Give the extent of all Plasmodium vivax-infected red blood cells.
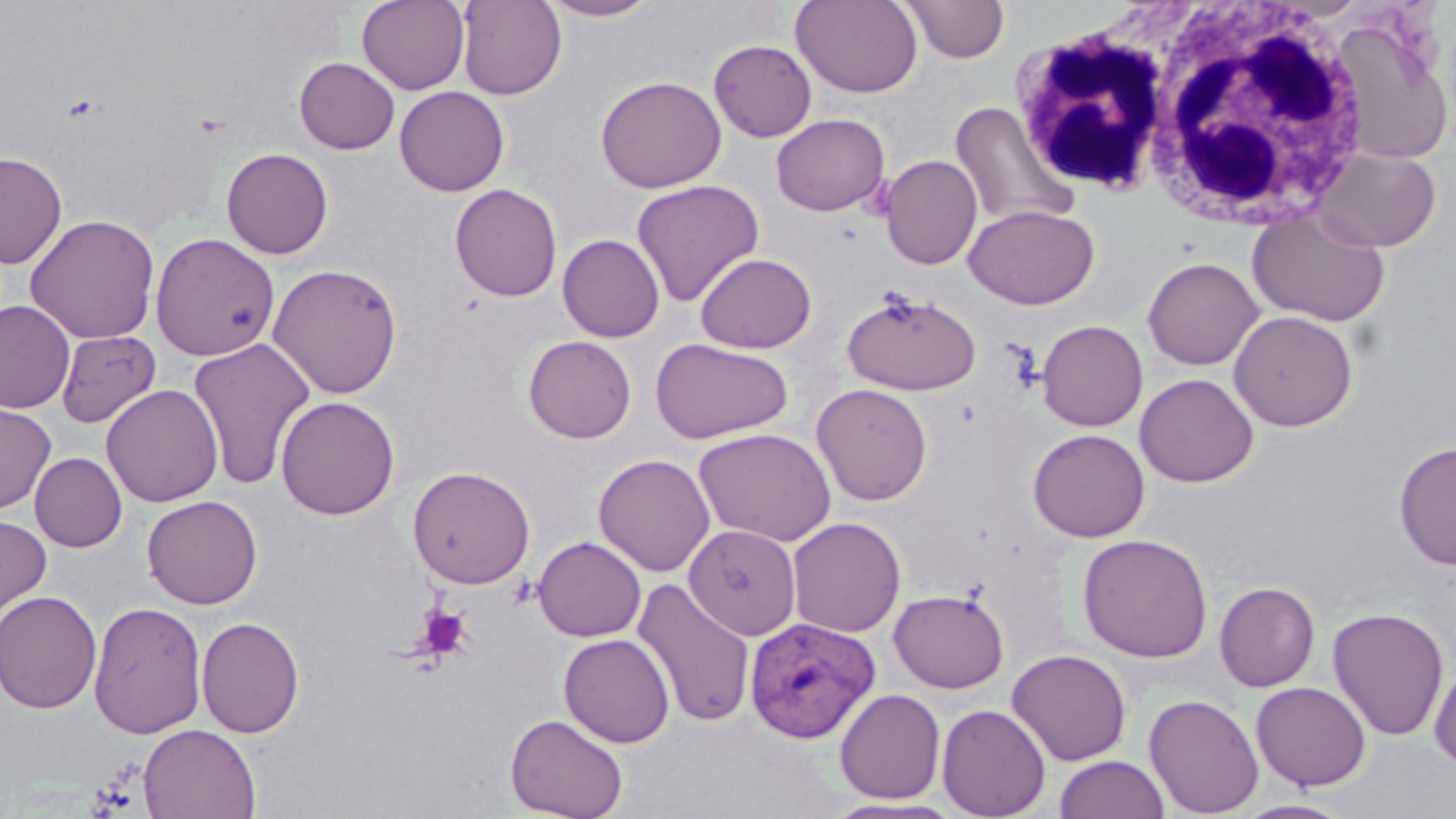

Approximate bounding boxes as [x1, y1, x2, y2] in pixels.
Plasmodium vivax-infected red blood cells: [744, 615, 883, 743].

{
  "slide_level_diagnosis": "Plasmodium vivax",
  "image_size": "1456×819 pixels",
  "magnification": "1000x",
  "uninfected_red_blood_cell_locations": "approximate bounding boxes as [x1, y1, x2, y2] in pixels: [357, 0, 470, 94], [456, 0, 567, 100], [539, 0, 662, 21], [900, 0, 1010, 63], [790, 1, 923, 98], [1328, 17, 1453, 165], [709, 39, 816, 142], [294, 57, 400, 154], [595, 75, 726, 193], [394, 86, 509, 196], [949, 101, 1076, 231], [771, 113, 890, 216], [1313, 146, 1441, 252], [221, 148, 333, 259], [0, 151, 67, 268], [879, 155, 983, 270], [631, 179, 765, 307], [449, 183, 563, 301], [964, 204, 1099, 310], [1246, 207, 1390, 327], [24, 213, 160, 344], [150, 232, 280, 361], [558, 234, 665, 342], [695, 252, 817, 354], [1142, 257, 1264, 370], [267, 262, 403, 399], [841, 289, 981, 397], [0, 300, 75, 414], [1228, 310, 1358, 431], [1037, 320, 1148, 431], [55, 330, 161, 429], [523, 335, 636, 443], [188, 337, 316, 491], [650, 337, 793, 444], [1134, 374, 1259, 487], [811, 383, 932, 506], [101, 384, 223, 507], [275, 395, 400, 519], [0, 399, 57, 514], [693, 427, 836, 547], [1028, 429, 1149, 543], [1394, 441, 1456, 570], [30, 452, 127, 552], [593, 453, 715, 577], [407, 465, 535, 589], [142, 495, 263, 609], [0, 514, 51, 625], [787, 516, 906, 637], [684, 524, 801, 640], [1077, 532, 1214, 663], [533, 536, 646, 641], [631, 577, 756, 729], [1214, 582, 1320, 692], [889, 588, 1009, 693], [0, 590, 102, 714], [88, 601, 208, 738], [1327, 606, 1450, 742], [196, 616, 305, 738], [559, 634, 675, 748], [1006, 648, 1132, 765], [1429, 660, 1456, 770], [1250, 681, 1371, 791], [834, 688, 945, 803], [1144, 695, 1264, 817], [936, 703, 1051, 819], [505, 713, 629, 819], [138, 724, 261, 819], [1054, 755, 1168, 818], [820, 797, 968, 819], [1233, 799, 1355, 818]",
  "white_blood_cell_locations": "approximate bounding boxes as [x1, y1, x2, y2] in pixels: [1136, 4, 1372, 232], [1008, 18, 1175, 198]",
  "platelet_locations": "approximate bounding boxes as [x1, y1, x2, y2] in pixels: [414, 605, 473, 661]",
  "field_of_view": "single",
  "preparation": "thin blood film",
  "modality": "optical microscopy",
  "stain": "May-Grünwald-Giemsa"
}